Identify the blood parasite species.
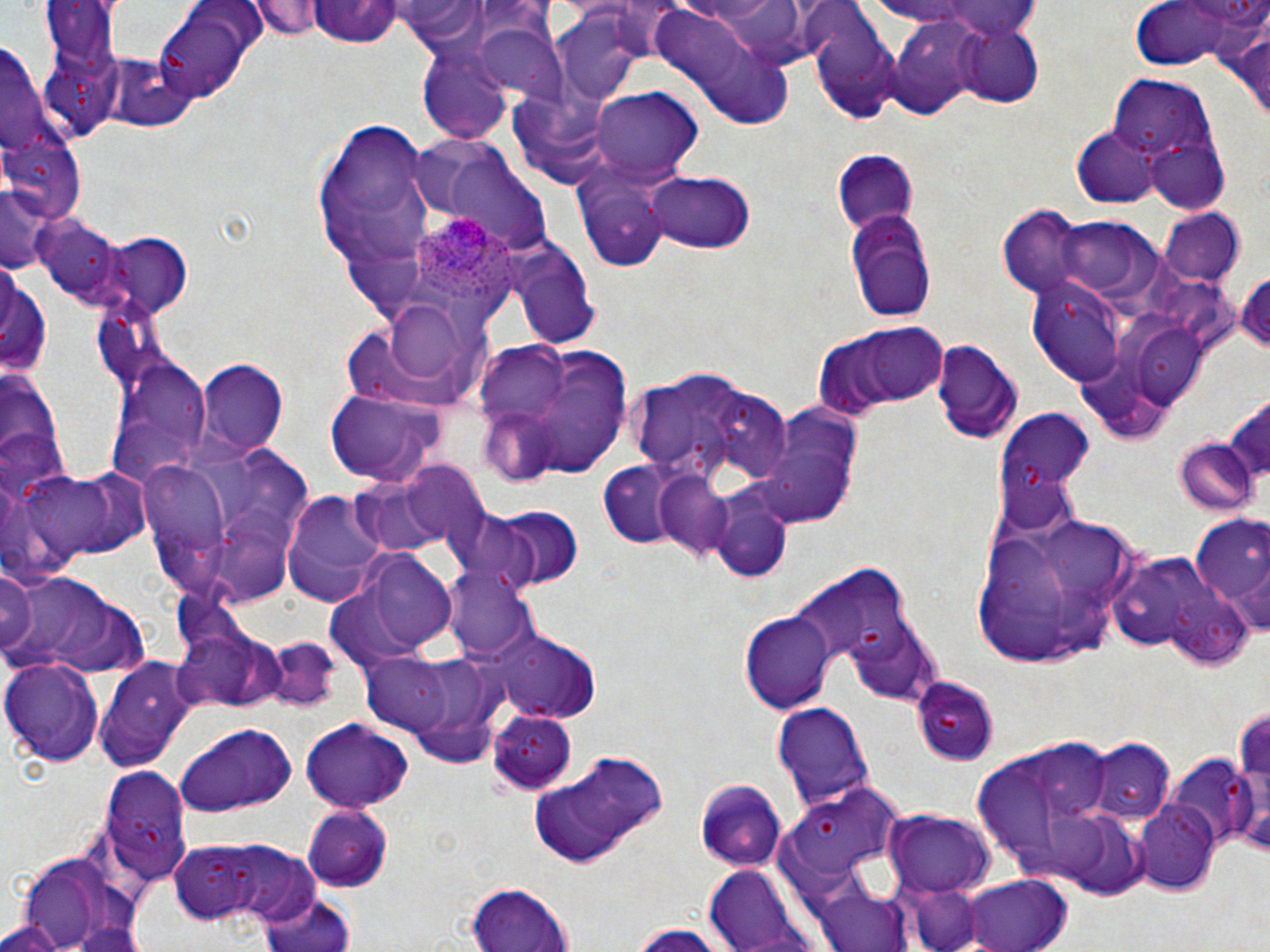

Plasmodium ovale.

Approximate bounding boxes as named x1/y1/x2/y2 corners in pixels. Plasmodium ovale-infected red blood cell locations: (x1=411, y1=214, x2=521, y2=307). Uninfected red blood cell locations: (x1=253, y1=1, x2=324, y2=41), (x1=927, y1=2, x2=1044, y2=40), (x1=1126, y1=2, x2=1269, y2=74), (x1=308, y1=4, x2=404, y2=51), (x1=151, y1=5, x2=267, y2=101), (x1=647, y1=6, x2=793, y2=123), (x1=552, y1=12, x2=648, y2=106), (x1=466, y1=19, x2=563, y2=104), (x1=882, y1=21, x2=985, y2=118), (x1=1227, y1=22, x2=1270, y2=124), (x1=812, y1=23, x2=899, y2=124), (x1=950, y1=25, x2=1042, y2=106), (x1=419, y1=45, x2=517, y2=145), (x1=1111, y1=77, x2=1217, y2=168), (x1=507, y1=88, x2=617, y2=189), (x1=591, y1=89, x2=700, y2=181), (x1=317, y1=123, x2=432, y2=262), (x1=1073, y1=128, x2=1160, y2=207), (x1=1142, y1=132, x2=1232, y2=214), (x1=832, y1=149, x2=918, y2=238), (x1=571, y1=161, x2=680, y2=271), (x1=640, y1=170, x2=758, y2=255), (x1=0, y1=185, x2=51, y2=274), (x1=844, y1=207, x2=939, y2=322), (x1=1157, y1=210, x2=1245, y2=286), (x1=33, y1=213, x2=126, y2=309), (x1=1041, y1=215, x2=1163, y2=303), (x1=95, y1=233, x2=192, y2=317), (x1=509, y1=242, x2=599, y2=346), (x1=0, y1=266, x2=51, y2=382), (x1=1236, y1=266, x2=1270, y2=356), (x1=1029, y1=283, x2=1125, y2=385), (x1=380, y1=297, x2=476, y2=386), (x1=834, y1=324, x2=951, y2=409), (x1=932, y1=337, x2=1022, y2=446), (x1=104, y1=353, x2=212, y2=483), (x1=198, y1=361, x2=289, y2=454), (x1=623, y1=361, x2=792, y2=490), (x1=0, y1=364, x2=66, y2=507), (x1=324, y1=389, x2=443, y2=484), (x1=1224, y1=391, x2=1270, y2=492), (x1=751, y1=401, x2=865, y2=532), (x1=1174, y1=439, x2=1257, y2=517), (x1=135, y1=447, x2=313, y2=608), (x1=395, y1=461, x2=493, y2=546), (x1=598, y1=462, x2=684, y2=547), (x1=15, y1=463, x2=151, y2=573), (x1=653, y1=472, x2=737, y2=560), (x1=359, y1=477, x2=456, y2=557), (x1=281, y1=489, x2=391, y2=605), (x1=712, y1=496, x2=792, y2=582), (x1=482, y1=503, x2=585, y2=593), (x1=967, y1=504, x2=1144, y2=668), (x1=1192, y1=518, x2=1270, y2=613), (x1=345, y1=548, x2=462, y2=660), (x1=795, y1=559, x2=921, y2=689), (x1=0, y1=567, x2=41, y2=662), (x1=444, y1=567, x2=539, y2=663), (x1=3, y1=568, x2=150, y2=679), (x1=741, y1=610, x2=835, y2=714), (x1=846, y1=618, x2=942, y2=705), (x1=173, y1=627, x2=284, y2=713), (x1=492, y1=631, x2=602, y2=726), (x1=262, y1=635, x2=342, y2=711), (x1=360, y1=654, x2=455, y2=734), (x1=2, y1=655, x2=102, y2=767), (x1=96, y1=661, x2=199, y2=771), (x1=913, y1=675, x2=999, y2=764), (x1=1234, y1=699, x2=1270, y2=845), (x1=771, y1=702, x2=872, y2=812), (x1=489, y1=708, x2=577, y2=794), (x1=299, y1=717, x2=414, y2=812), (x1=176, y1=722, x2=297, y2=818), (x1=971, y1=738, x2=1128, y2=877), (x1=1084, y1=739, x2=1174, y2=826), (x1=1203, y1=740, x2=1268, y2=852), (x1=523, y1=751, x2=667, y2=868), (x1=1168, y1=760, x2=1253, y2=854), (x1=98, y1=763, x2=194, y2=884), (x1=693, y1=778, x2=787, y2=870), (x1=784, y1=782, x2=908, y2=880), (x1=1134, y1=800, x2=1219, y2=893), (x1=302, y1=804, x2=393, y2=891), (x1=1058, y1=811, x2=1150, y2=899), (x1=886, y1=812, x2=994, y2=895), (x1=169, y1=841, x2=262, y2=925), (x1=228, y1=846, x2=322, y2=927), (x1=707, y1=865, x2=809, y2=949), (x1=953, y1=875, x2=1074, y2=952), (x1=905, y1=883, x2=982, y2=952), (x1=465, y1=884, x2=571, y2=952), (x1=814, y1=886, x2=914, y2=952), (x1=257, y1=888, x2=359, y2=952), (x1=2, y1=920, x2=69, y2=951), (x1=634, y1=925, x2=722, y2=952). 1000x magnification. One field of a larger specimen. Image is 1270×952 pixels. Thin blood smear. Optical microscopy. May-Grünwald-Giemsa-stained preparation.